Identify the cell.
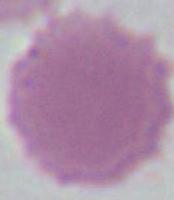
An erythrocyte.

Summary:
  - Modality: photomicrograph
  - Magnification: 1000x